State which parasite is depicted.
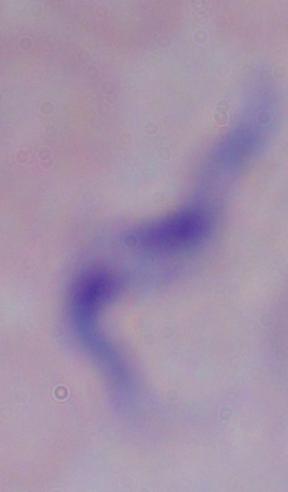
This is a trypanosome.

{
  "magnification": "1000x",
  "modality": "micrograph"
}